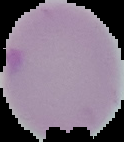
image type = segmented cell region with the area outside set to black
preparation = thin blood film
image size = 124×142 pixels
result = no Plasmodium parasites seen